Identify the preparation type.
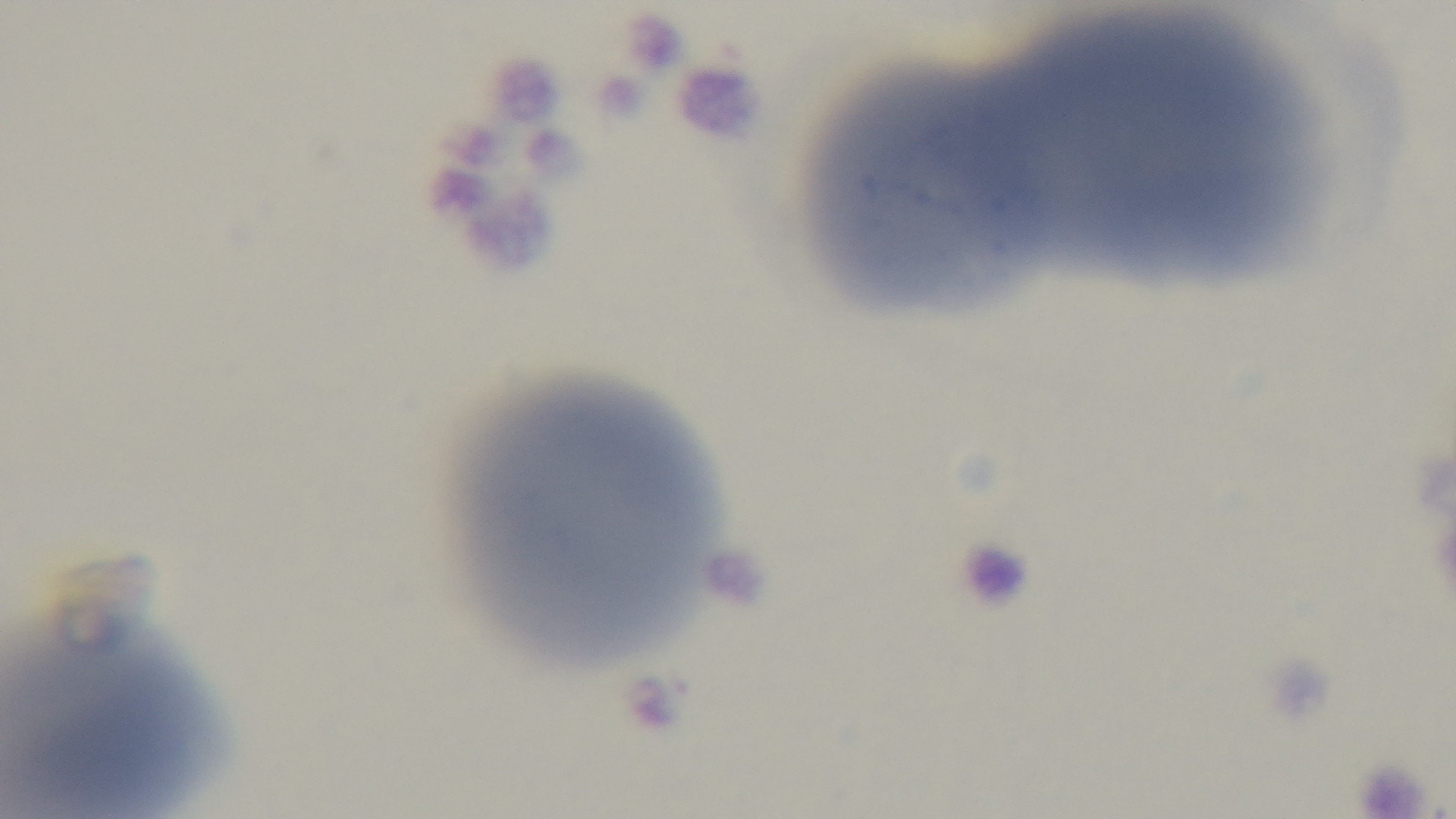

A thin smear.

Mounted 4K digital camera. Single field of view. 100x oil-immersion objective. Giemsa-stained. Malaria status: negative. Photomicrograph.